State which cell type is depicted.
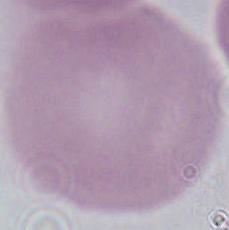

An erythrocyte.

1000x magnification. Micrograph.